Assess the morphology of the erythrocytes.
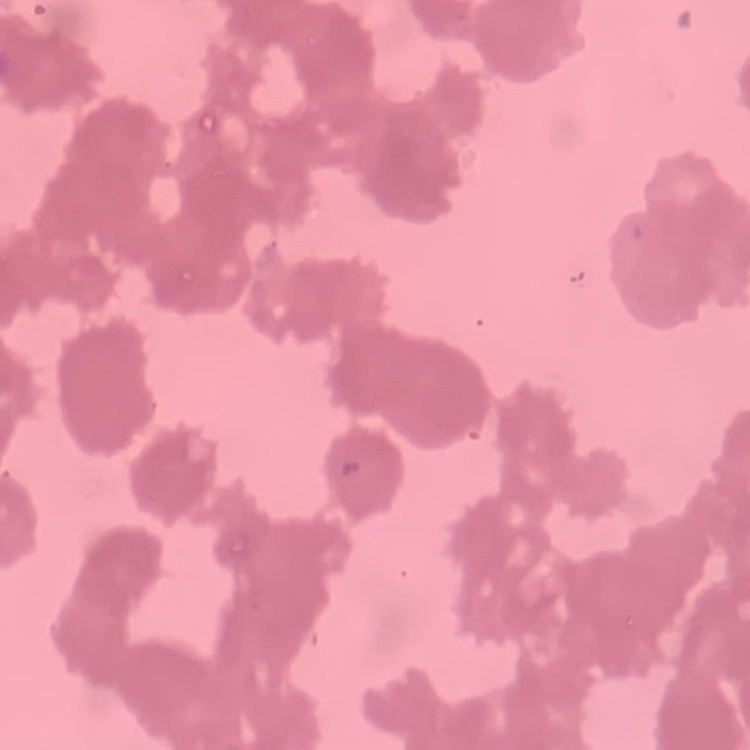
Rouleaux formation.

stain: Field's or Giemsa
preparation: thin peripheral smear
image_type: one tile cut from a larger photomicrograph